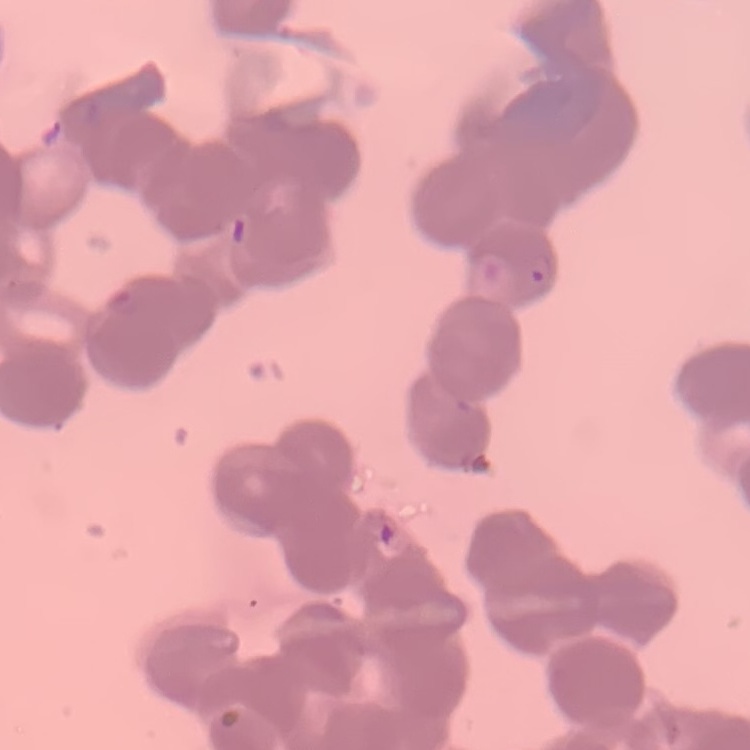 The red blood cells exhibit rouleaux formation. One tile cut from a larger photomicrograph. Stained with either Field's or Giemsa. Thin peripheral smear.